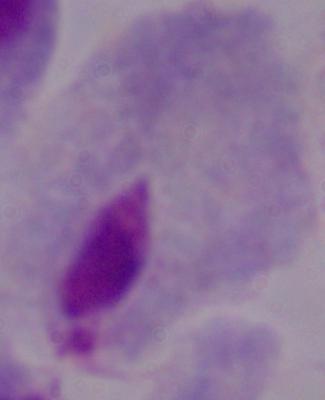
A trichomonad is seen. Micrograph. Captured at 1000x magnification.